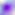 Captured at 400x magnification. Toxoplasma gondii is shown. Photomicrograph.